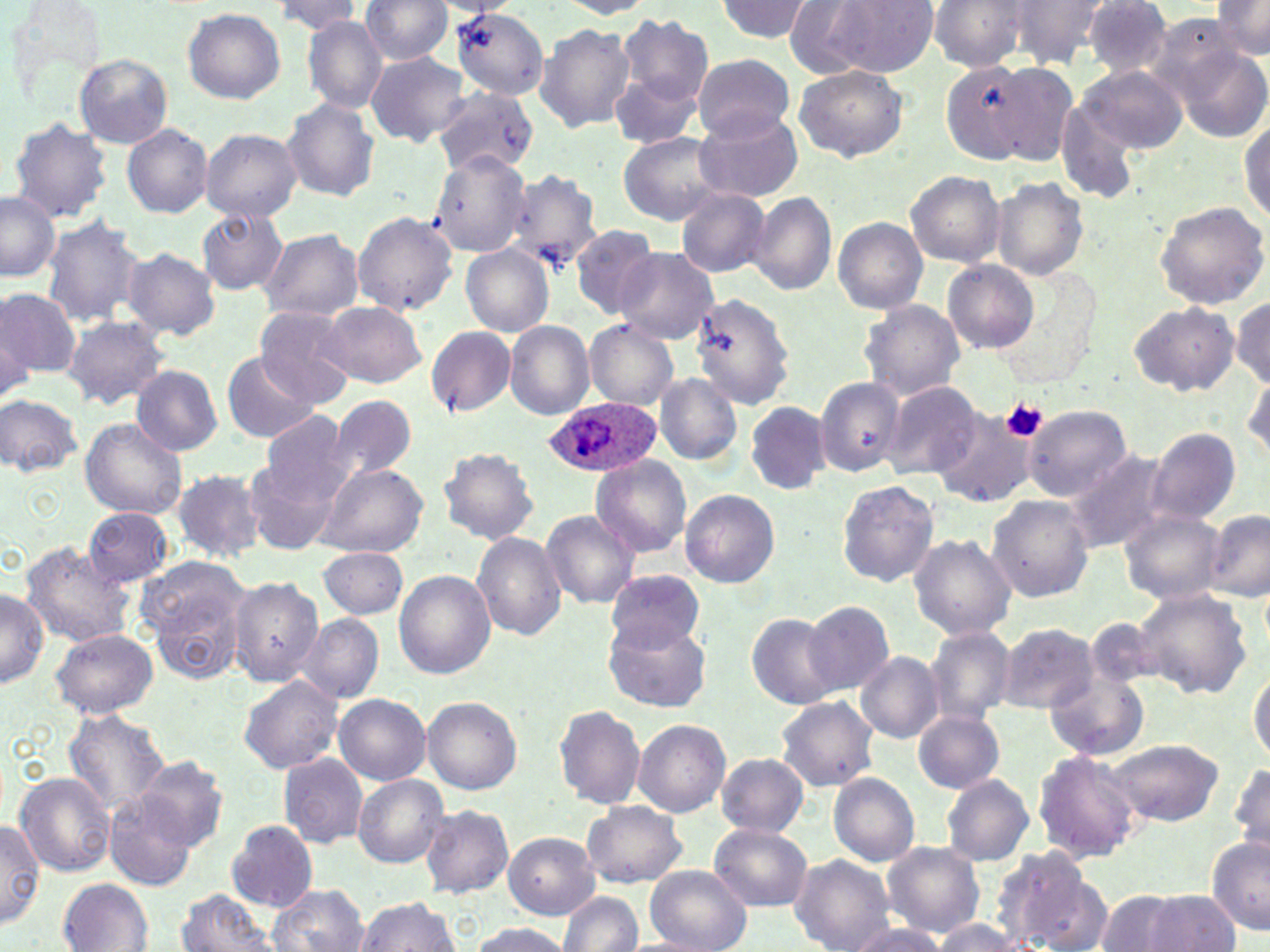
Summary:
  - Coordinate format: approximate bounding boxes as (x1,y1)-(x2,y2) corner pairs in pixels
  - Platelet locations: (1001,399)-(1048,444)
  - Plasmodium ovale-infected red blood cell locations: (545,396)-(660,479)
  - Uninfected red blood cell locations: (358,0)-(452,64), (558,0)-(656,19), (717,0)-(815,44), (782,0)-(895,78), (1007,0)-(1110,68), (825,1)-(937,77), (928,1)-(1034,72), (1080,1)-(1173,78), (1211,1)-(1269,59), (273,2)-(362,34), (182,7)-(284,103), (453,7)-(550,100), (618,13)-(712,105), (303,16)-(386,113), (534,23)-(637,133), (1177,45)-(1268,146), (364,52)-(471,146), (74,54)-(172,149), (691,56)-(793,139), (943,61)-(1031,163), (983,61)-(1083,164), (1078,63)-(1186,154), (794,65)-(907,162), (609,69)-(704,150), (433,87)-(539,176), (281,97)-(381,202), (695,110)-(803,204), (1239,111)-(1269,226), (8,119)-(112,222), (123,125)-(214,217), (201,128)-(302,222), (618,133)-(724,225), (429,149)-(532,256), (506,169)-(603,274), (905,169)-(1005,267), (992,179)-(1088,278), (676,188)-(770,277), (748,192)-(837,295), (0,193)-(61,281), (1153,200)-(1269,310), (195,208)-(287,295), (352,211)-(459,315), (40,215)-(147,328), (833,216)-(928,313), (570,223)-(660,318), (258,228)-(364,322), (461,245)-(555,336), (614,247)-(720,342), (120,248)-(221,340), (945,261)-(1037,352), (0,287)-(77,380), (686,294)-(793,415), (1232,296)-(1269,387), (317,301)-(426,386), (860,301)-(965,400), (1128,302)-(1238,397), (252,306)-(355,404), (0,313)-(35,399), (61,316)-(170,410), (585,319)-(678,408), (504,321)-(595,419), (426,325)-(517,417), (220,350)-(323,443), (131,366)-(224,456), (1244,367)-(1270,463), (654,373)-(742,464), (816,376)-(907,476), (881,380)-(986,480), (0,394)-(83,477), (323,395)-(417,487), (296,397)-(414,552), (744,402)-(829,495), (1024,405)-(1132,502), (259,409)-(352,509), (930,411)-(1038,510), (79,418)-(187,520), (1147,429)-(1241,523), (436,447)-(540,545), (1064,447)-(1173,554), (590,455)-(693,558), (246,459)-(340,554), (318,462)-(428,558), (170,469)-(268,561), (835,478)-(940,587), (679,490)-(781,587), (987,495)-(1093,603), (83,507)-(173,585), (1120,507)-(1226,605), (540,510)-(641,609), (1205,510)-(1270,602), (471,531)-(566,641), (908,534)-(1016,641), (19,541)-(137,650), (318,547)-(408,619), (139,557)-(253,684), (608,569)-(705,656), (394,570)-(496,680), (226,575)-(320,686), (0,587)-(48,687), (1134,588)-(1252,701), (802,599)-(892,696), (746,612)-(843,710), (296,614)-(384,705), (603,617)-(712,714), (993,623)-(1098,712), (923,626)-(1019,726), (50,628)-(158,719), (854,651)-(944,743), (1043,667)-(1149,763), (1249,667)-(1270,765), (238,674)-(344,774), (334,694)-(432,783), (423,695)-(522,794), (775,696)-(879,791), (553,705)-(646,809), (913,709)-(1005,794), (63,710)-(170,814), (632,718)-(730,817), (1109,739)-(1222,824), (1032,750)-(1142,863), (716,753)-(810,834), (277,754)-(369,848), (135,755)-(230,854), (1230,758)-(1270,860), (14,772)-(117,877), (828,774)-(921,865), (941,774)-(1035,866), (353,775)-(449,867), (104,792)-(199,890), (581,801)-(687,888), (420,805)-(514,898), (0,819)-(43,929), (227,820)-(318,910), (709,823)-(814,911), (503,832)-(599,919), (1206,835)-(1269,934), (658,837)-(799,935), (883,842)-(985,937), (989,846)-(1099,952), (788,855)-(897,952), (645,865)-(751,952), (58,878)-(154,950), (267,884)-(371,952), (175,889)-(277,952), (1095,890)-(1183,952), (1143,890)-(1243,951), (560,892)-(643,952), (353,896)-(461,951), (846,917)-(948,952), (932,919)-(1020,952), (466,921)-(573,952)
  - Slide-level diagnosis: Plasmodium ovale
  - Image size: 1270×952 pixels
  - Magnification: 1000x
  - Preparation: thin blood film
  - Modality: light microscopy
  - Stain: May-Grünwald-Giemsa
  - Field of view: single